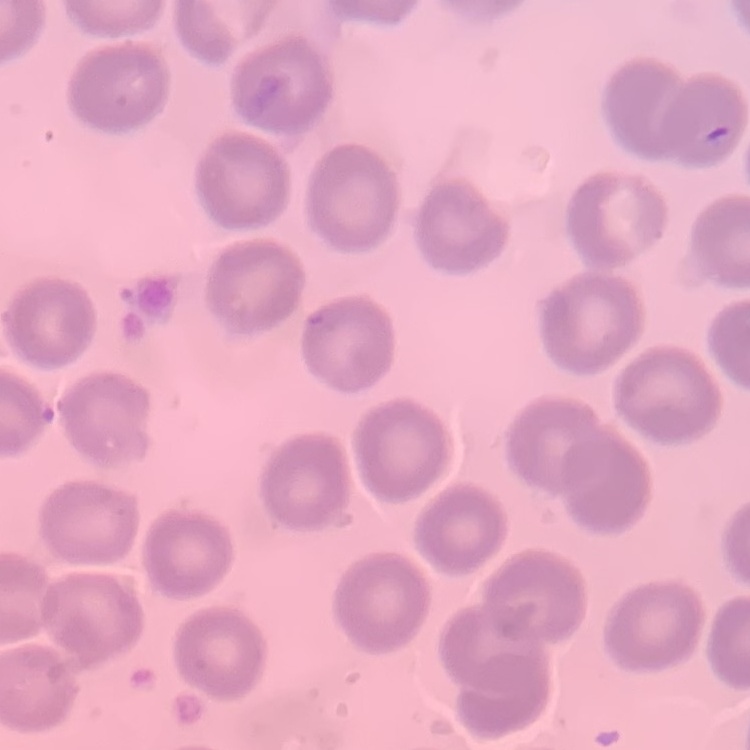

Summary:
  - Red blood cell morphology: no rouleaux formation
  - Stain: Field's or Giemsa
  - Image type: square crop of a larger photomicrograph
  - Preparation: thin blood film